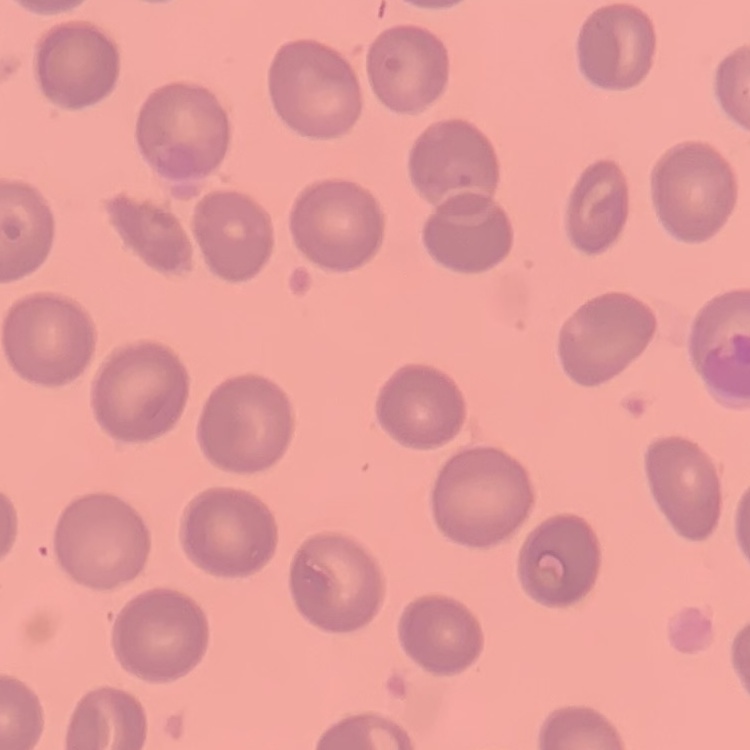

Summary:
  - Erythrocyte morphology: no rouleaux formation
  - Preparation: thin blood smear
  - Stain: Field's or Giemsa
  - Image type: one tile cut from a larger photomicrograph